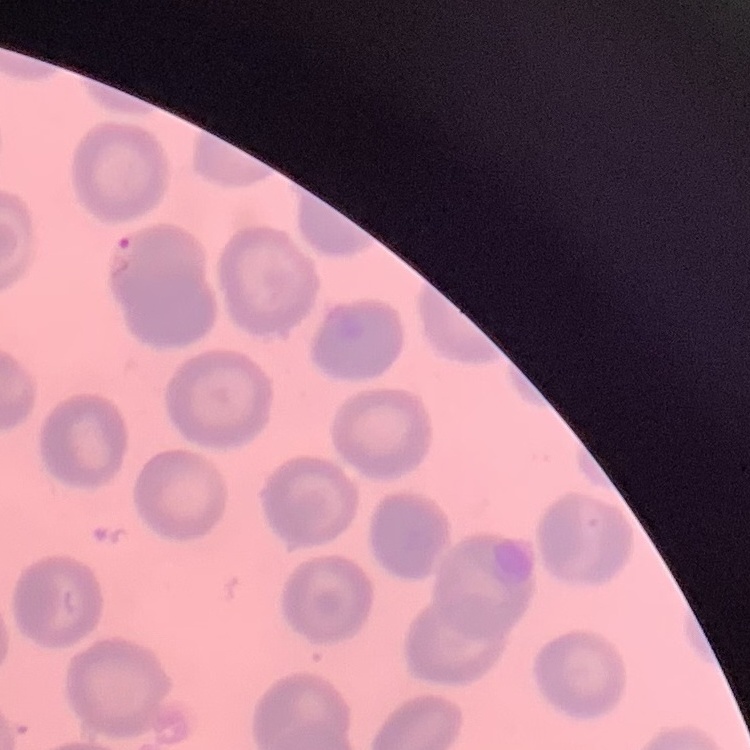

erythrocyte morphology = no rouleaux formation
stain = Field's or Giemsa
preparation = thin blood smear
image type = one tile cut from a larger photomicrograph